Identify the parasite.
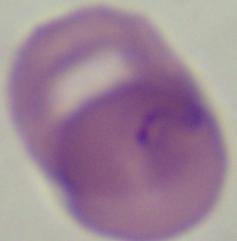

Babesia.

modality = photomicrograph
magnification = 1000x